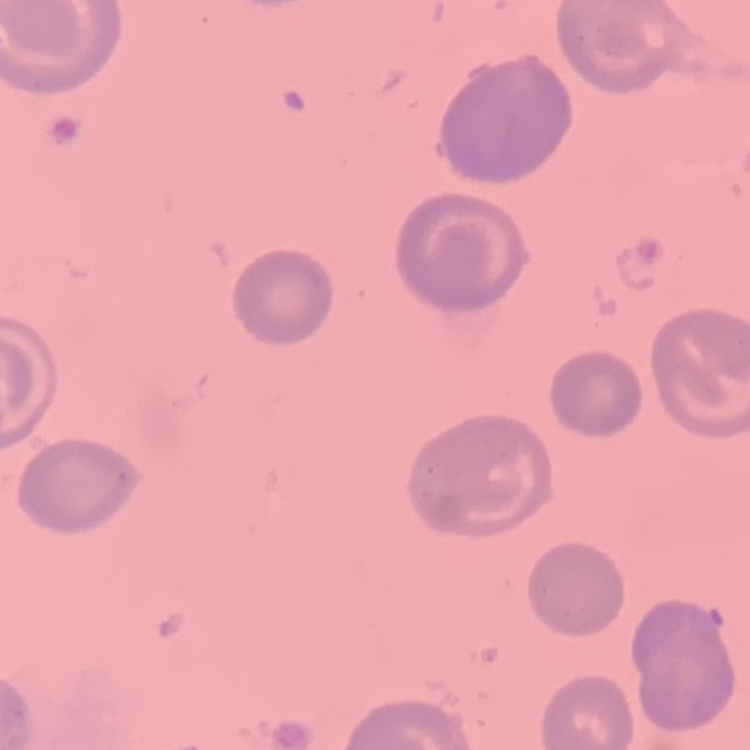

Summary:
  - Erythrocyte morphology: no rouleaux formation
  - Image type: square crop of a larger photomicrograph
  - Preparation: thin blood film
  - Stain: Field's or Giemsa